Locate leukocytes (white blood cells).
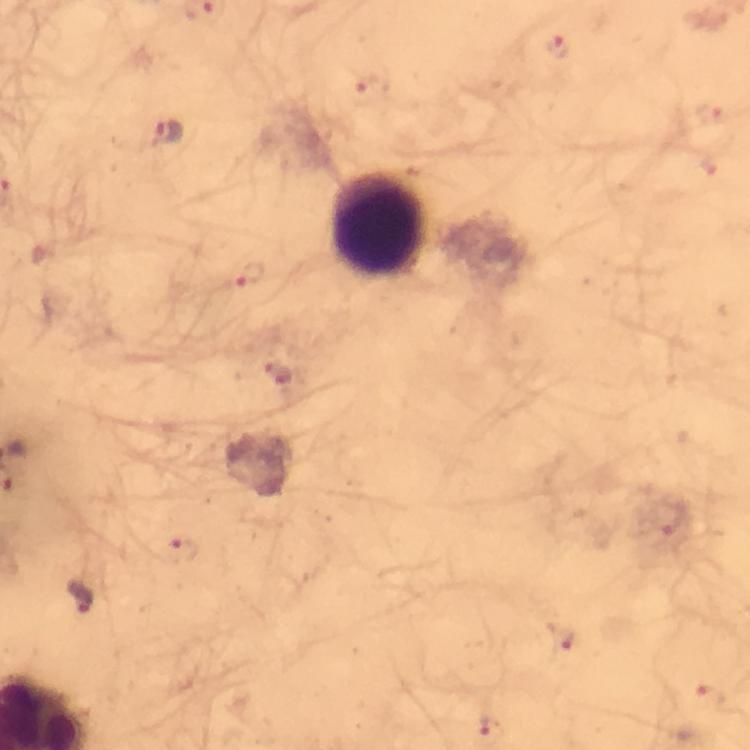

Approximate centers as (x, y) in pixels.
Leukocytes: (379, 225).

Summary:
  - Plasmodium parasite locations: (555, 50), (365, 88), (708, 112), (166, 131), (251, 278), (281, 374), (671, 518), (184, 555), (80, 599), (563, 638), (708, 698), (493, 726)
  - Capture: smartphone photograph through a microscope
  - Magnification: 100x
  - Image size: 750×750 pixels
  - Cropped from: a single field of view
  - Context: from a diagnostic examination for malaria
  - Stain: Giemsa
  - Preparation: thick blood smear
  - Immersion oil: applied